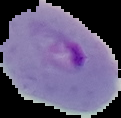
image_size: 121×118 pixels
image_type: segmented cell region on a black background
malaria_status: parasitized
preparation: thin blood smear